Describe the morphology of the red blood cells.
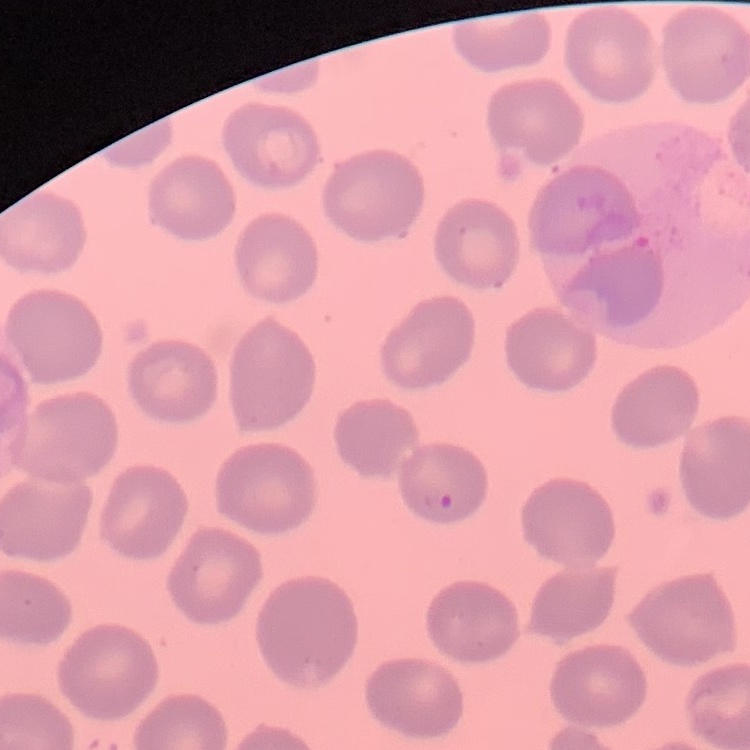

No rouleaux formation.

image type = square crop of a larger photomicrograph
stain = Field's or Giemsa
preparation = thin blood film